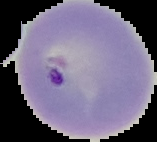

Summary:
  - Malaria status: parasitized
  - Image size: 157×142 pixels
  - Image type: segmented cell region on a black background
  - Preparation: thin blood smear